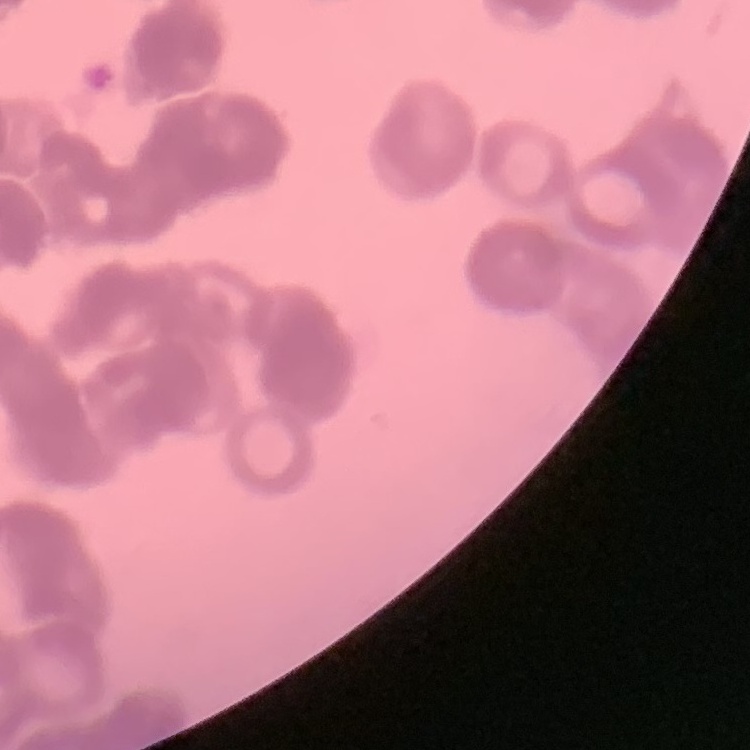
{
  "red_blood_cell_morphology": "rouleaux formation",
  "image_type": "square crop of a larger photomicrograph",
  "stain": "Field's or Giemsa",
  "preparation": "thin peripheral smear"
}